Report the malaria status of this cell.
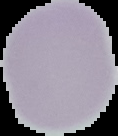

It is uninfected.

Image is 118×136 pixels. Segmented cell region on a black background. From a thin blood smear.